Point out each leukocyte.
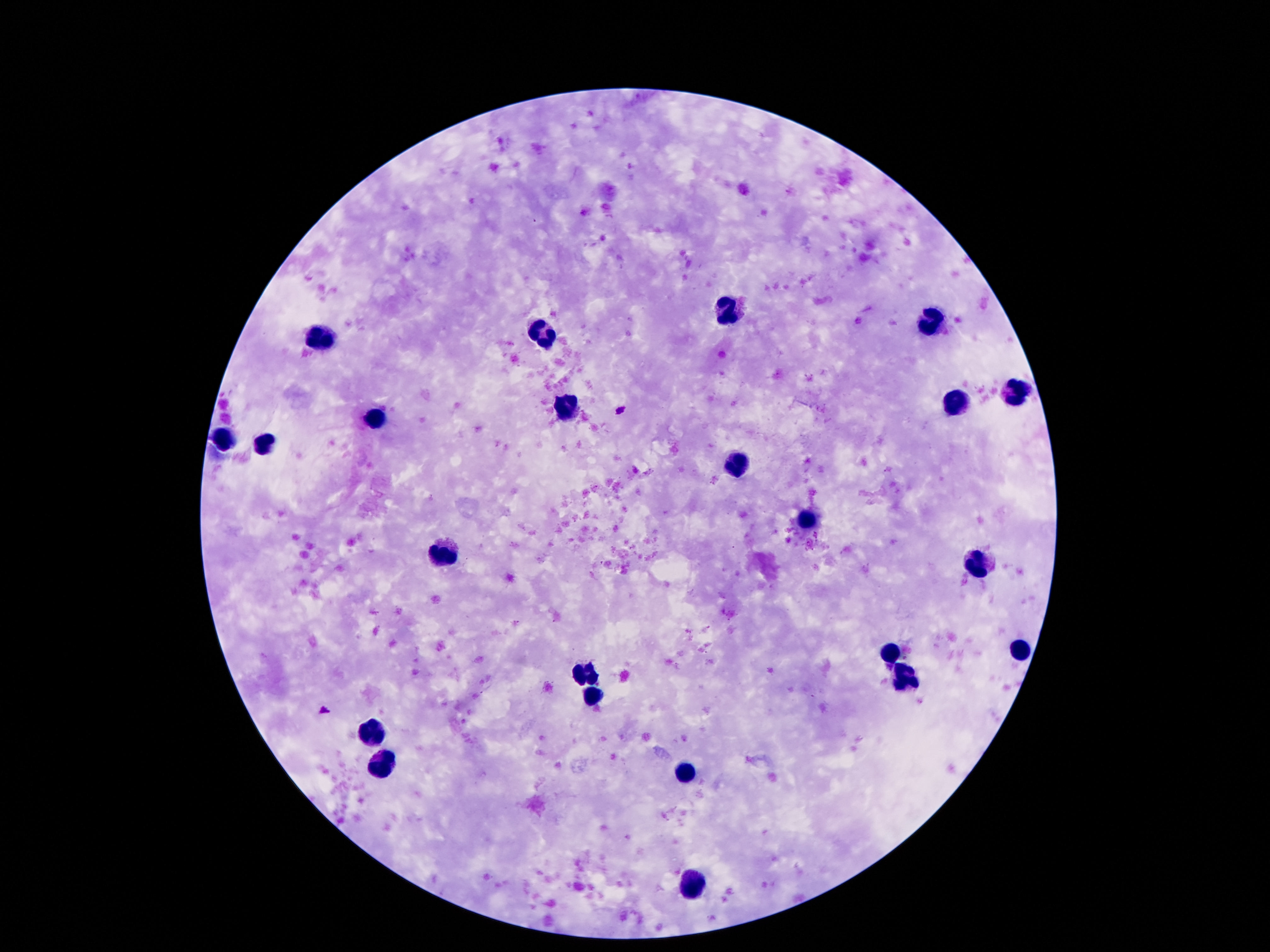

Approximate centers as {x, y} in pixels.
Leukocytes: {728, 315}, {930, 322}, {539, 333}, {323, 340}, {1018, 393}, {952, 403}, {566, 406}, {373, 418}, {223, 439}, {262, 444}, {739, 468}, {807, 525}, {441, 557}, {977, 561}, {891, 650}, {1018, 655}, {584, 673}, {902, 675}, {591, 695}, {371, 732}, {382, 766}, {689, 771}, {693, 882}.

stain = Giemsa
field of view = single
capture = smartphone camera through the microscope eyepiece
preparation = thick peripheral-blood smear
magnification = 100x
image size = 1270×952 pixels
patient malaria status = negative